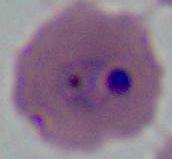 A Plasmodium parasite is seen. Photomicrograph. 400x or 1000x magnification.